Assess the morphology of the red blood cells.
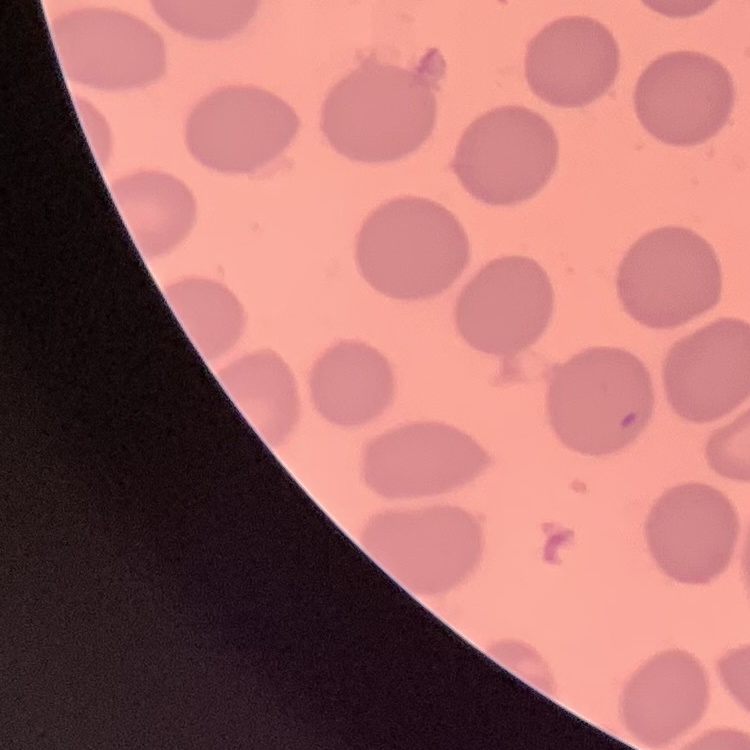
They show no rouleaux formation.

Summary:
  - Image type: one tile cut from a larger photomicrograph
  - Preparation: thin blood smear
  - Stain: Field's or Giemsa